Assess this cell for malaria.
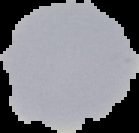
It is uninfected.

Image is 139×133 pixels. Cell region segmented out of the field of view; the surrounding area is masked to black. From a thin blood film.